Classify this cell by malaria status.
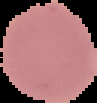

Uninfected.

preparation = thin blood smear
image type = segmented cell region with the area outside set to black
image size = 97×103 pixels